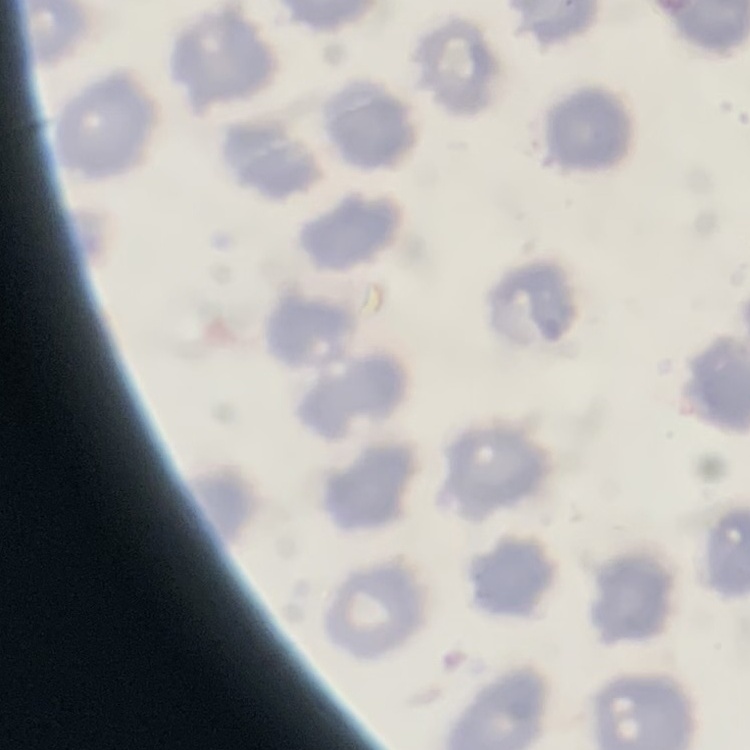

Summary:
  - Red blood cell morphology: no rouleaux formation
  - Preparation: thin blood smear
  - Stain: Field's or Giemsa
  - Image type: square crop of a larger photomicrograph